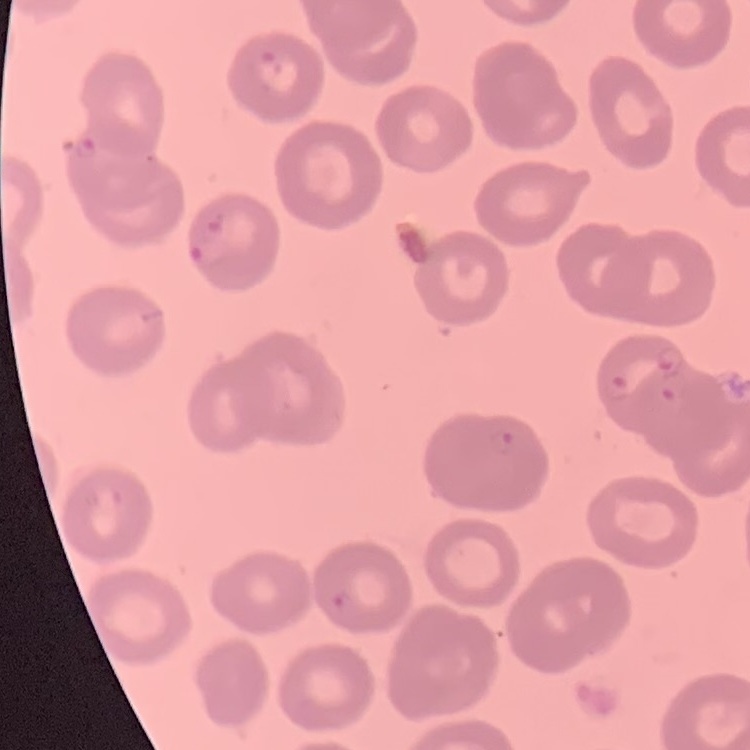

The red blood cells show no rouleaux formation. Thin peripheral smear. Square crop of a larger photomicrograph. Field's or Giemsa stain.